Identify the parasite.
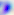
This is Toxoplasma gondii.

Micrograph. 400x magnification.